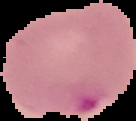

image type = cell region segmented out of the field of view; surrounding area masked to black
image size = 136×121 pixels
malaria status = parasitized
preparation = thin blood film